Report the malaria status.
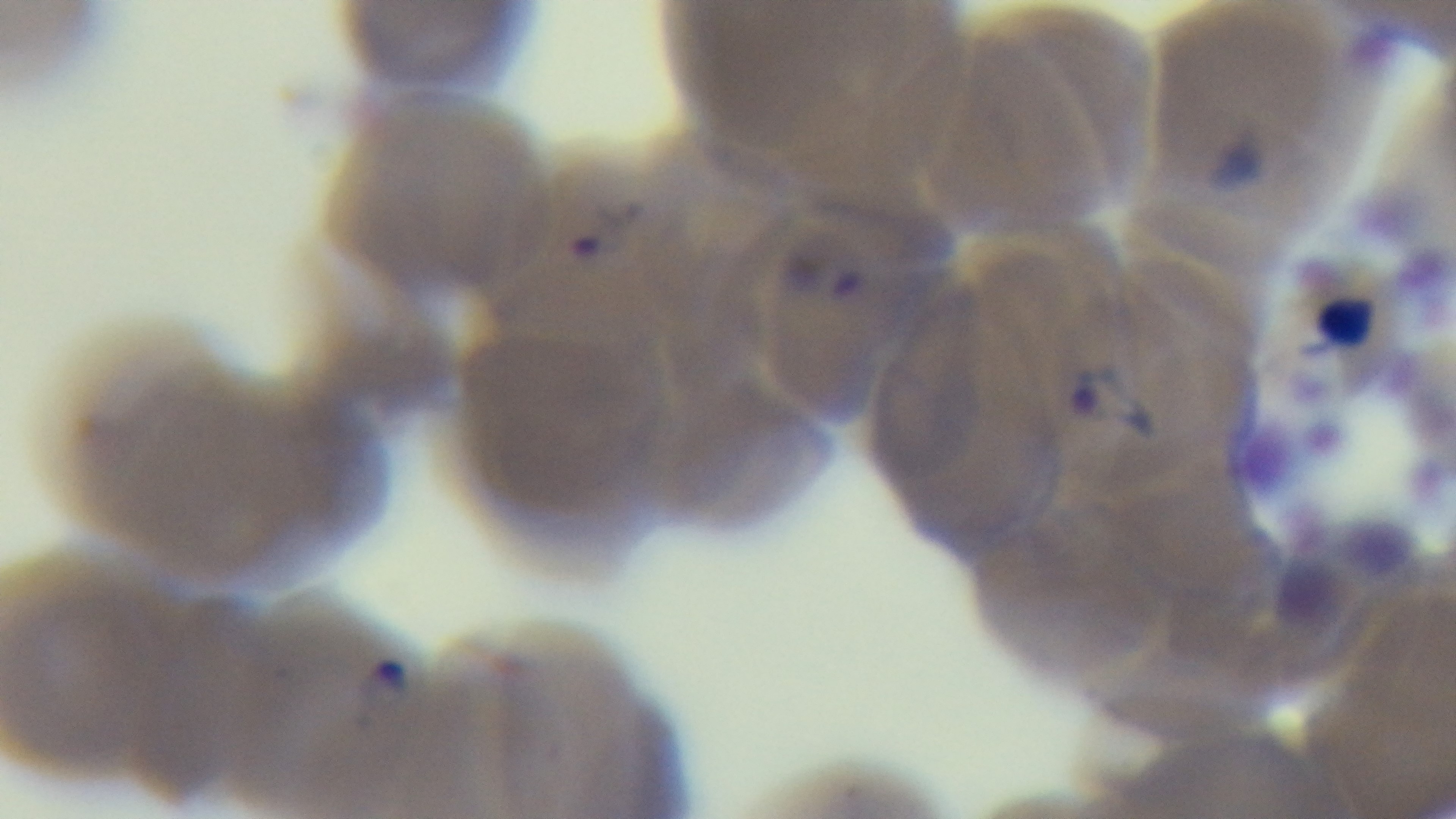
It is infected.

Summary:
  - Stain: Giemsa
  - Modality: light microscopy
  - Field of view: single
  - Capture: mounted 4K digital camera
  - Preparation: thin
  - Objective: 100x oil immersion